Evaluate for Plasmodium parasites.
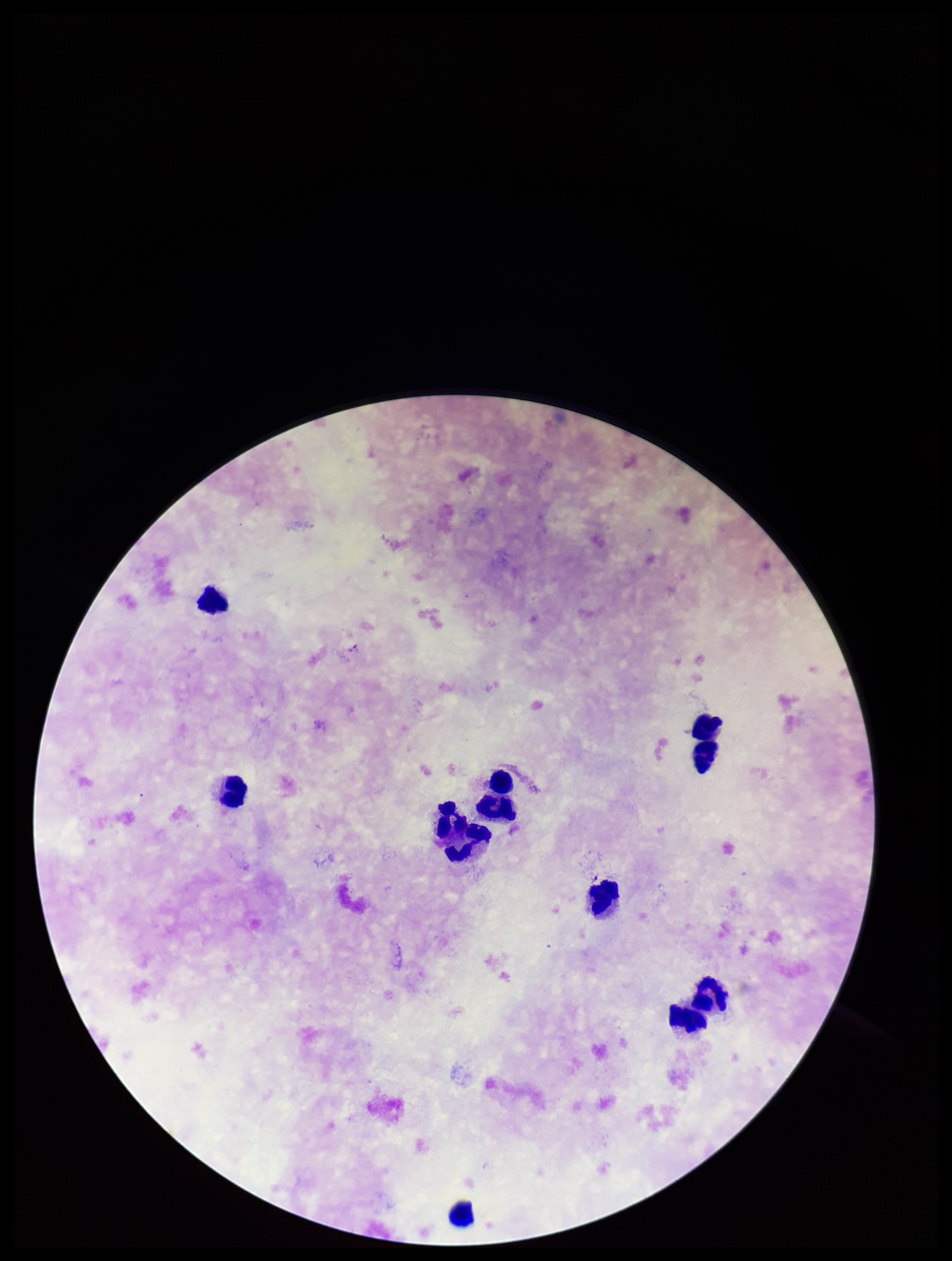

None identified.

{
  "stain": "Giemsa",
  "species_reported_for_this_patient": "Plasmodium falciparum",
  "preparation": "thick",
  "image_size": "952×1261 pixels",
  "parasite_count": 0,
  "capture": "smartphone photograph through the microscope eyepiece",
  "leukocyte_count": 12,
  "field_of_view": "one from this slide",
  "patient_malaria_status": "infected"
}